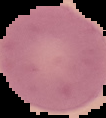

Summary:
  - Malaria status: uninfected
  - Image size: 106×118 pixels
  - Preparation: thin blood film
  - Image type: cell region segmented out of the field of view; surrounding area masked to black